Describe the morphology of the red blood cells.
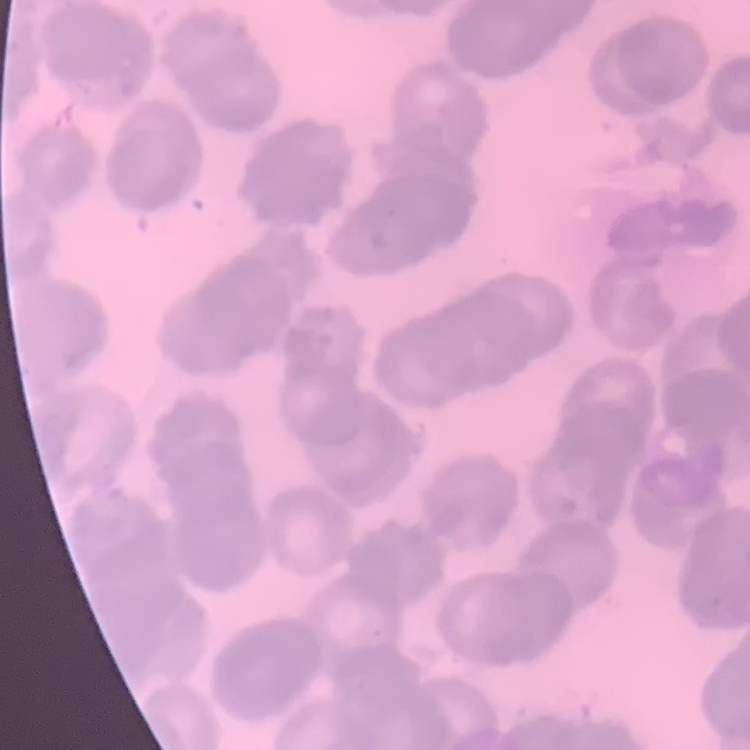

Rouleaux formation.

Summary:
  - Stain: Field's or Giemsa
  - Preparation: thin blood smear
  - Image type: one tile cut from a larger photomicrograph